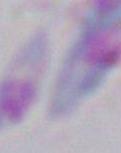

Captured at 1000x magnification. Micrograph. Toxoplasma gondii is shown.